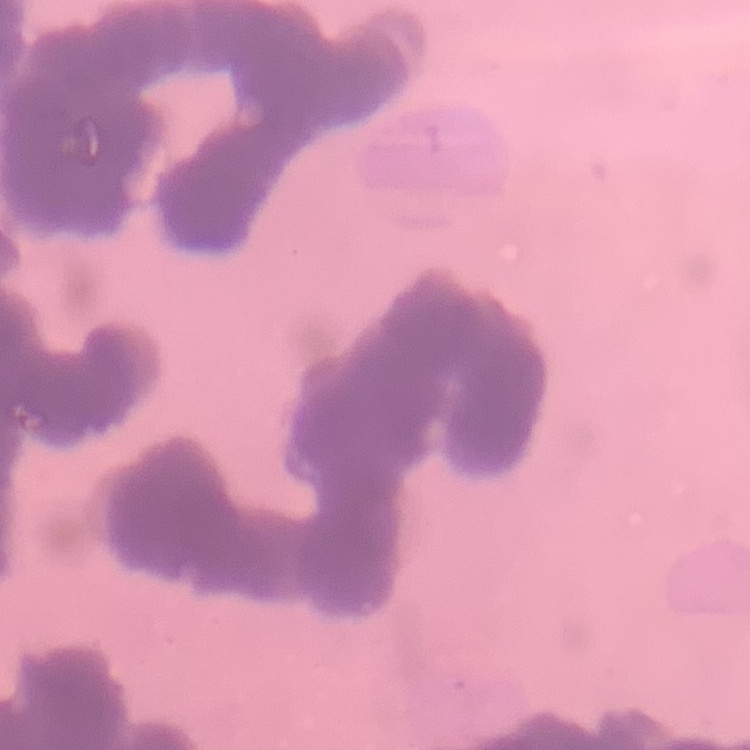
red blood cell morphology = rouleaux formation
stain = Field's or Giemsa
image type = square crop of a larger photomicrograph
preparation = thin peripheral smear